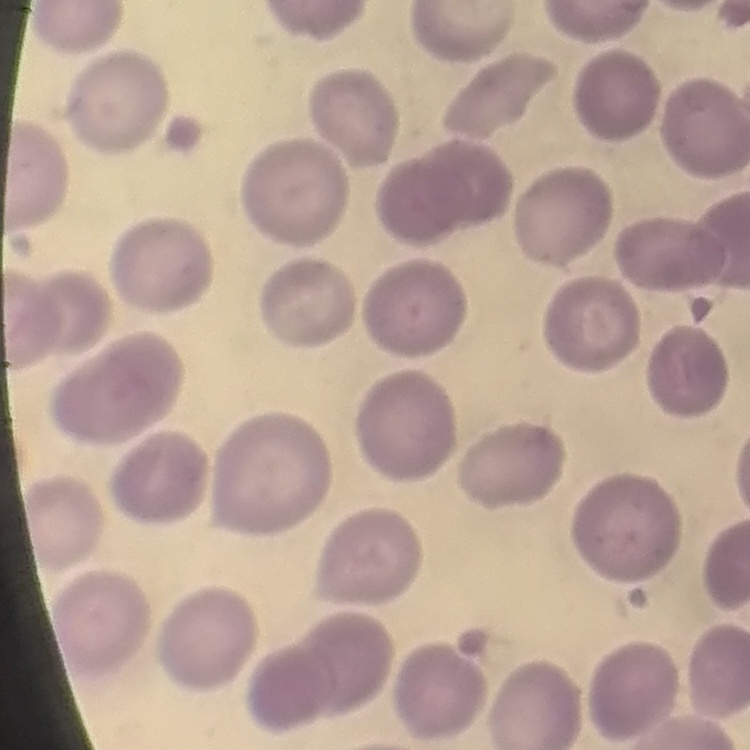
Summary:
  - Red blood cell morphology: no rouleaux formation
  - Stain: Field's or Giemsa
  - Image type: square crop of a larger photomicrograph
  - Preparation: thin blood smear